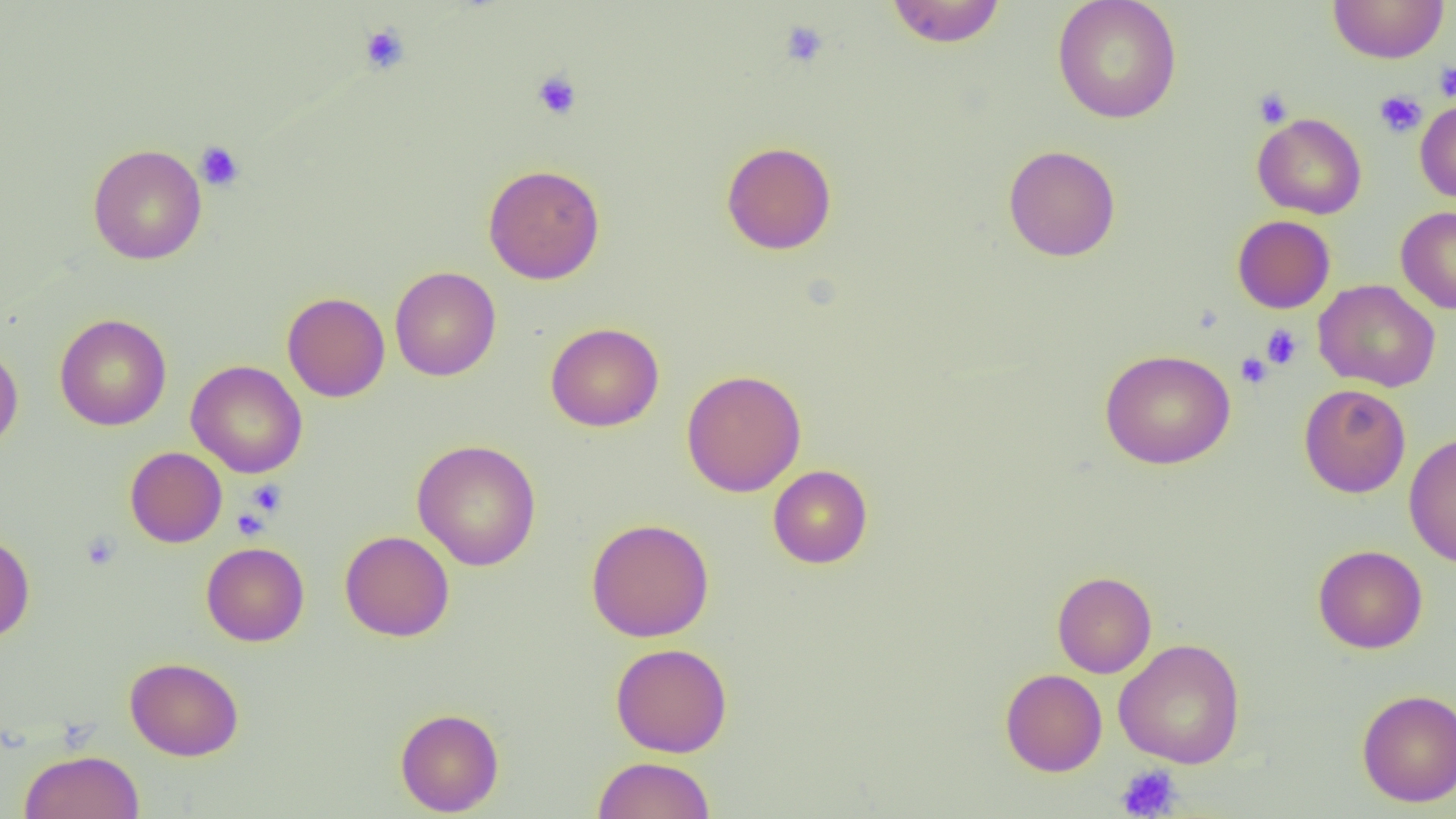
Approximate bounding boxes as (x1, y1, x2, y2) in pixels. Platelet locations: (779, 20, 830, 68), (359, 22, 410, 74), (1434, 61, 1456, 102), (531, 70, 583, 121), (1253, 87, 1294, 128), (1374, 89, 1427, 138), (194, 141, 245, 191), (1261, 325, 1302, 369), (1235, 352, 1272, 388), (246, 479, 287, 517), (231, 507, 270, 540), (80, 531, 121, 571), (1115, 764, 1182, 818). Uninfected red blood cell locations: (885, 0, 1006, 48), (1052, 0, 1183, 124), (1328, 0, 1449, 64), (1415, 98, 1456, 203), (1253, 113, 1367, 219), (721, 140, 837, 254), (88, 144, 207, 265), (1003, 144, 1121, 261), (483, 164, 604, 284), (1396, 206, 1456, 314), (1232, 215, 1336, 313), (389, 266, 501, 381), (1314, 279, 1441, 392), (282, 292, 390, 402), (55, 314, 171, 430), (545, 322, 663, 432), (0, 343, 23, 453), (1100, 348, 1235, 469), (186, 360, 307, 478), (681, 369, 806, 497), (1298, 383, 1411, 498), (1404, 432, 1456, 568), (412, 439, 541, 570), (125, 446, 227, 547), (768, 465, 872, 568), (586, 518, 714, 642), (340, 530, 454, 641), (0, 532, 35, 642), (201, 542, 309, 646), (1313, 544, 1428, 653), (1052, 571, 1157, 678), (1114, 638, 1245, 769), (611, 642, 732, 757), (125, 657, 244, 761), (1001, 668, 1107, 776), (1357, 689, 1456, 807), (395, 708, 504, 816), (19, 750, 144, 819), (593, 756, 715, 819). Slide-level diagnosis: negative for blood parasites. Single field of view. 1000x magnification. Image is 1456×819 pixels. Optical microscopy. Thin blood film.